Identify the cell.
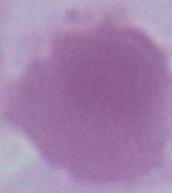

This is an erythrocyte.

Photomicrograph. 1000x magnification.